State the blood parasite species.
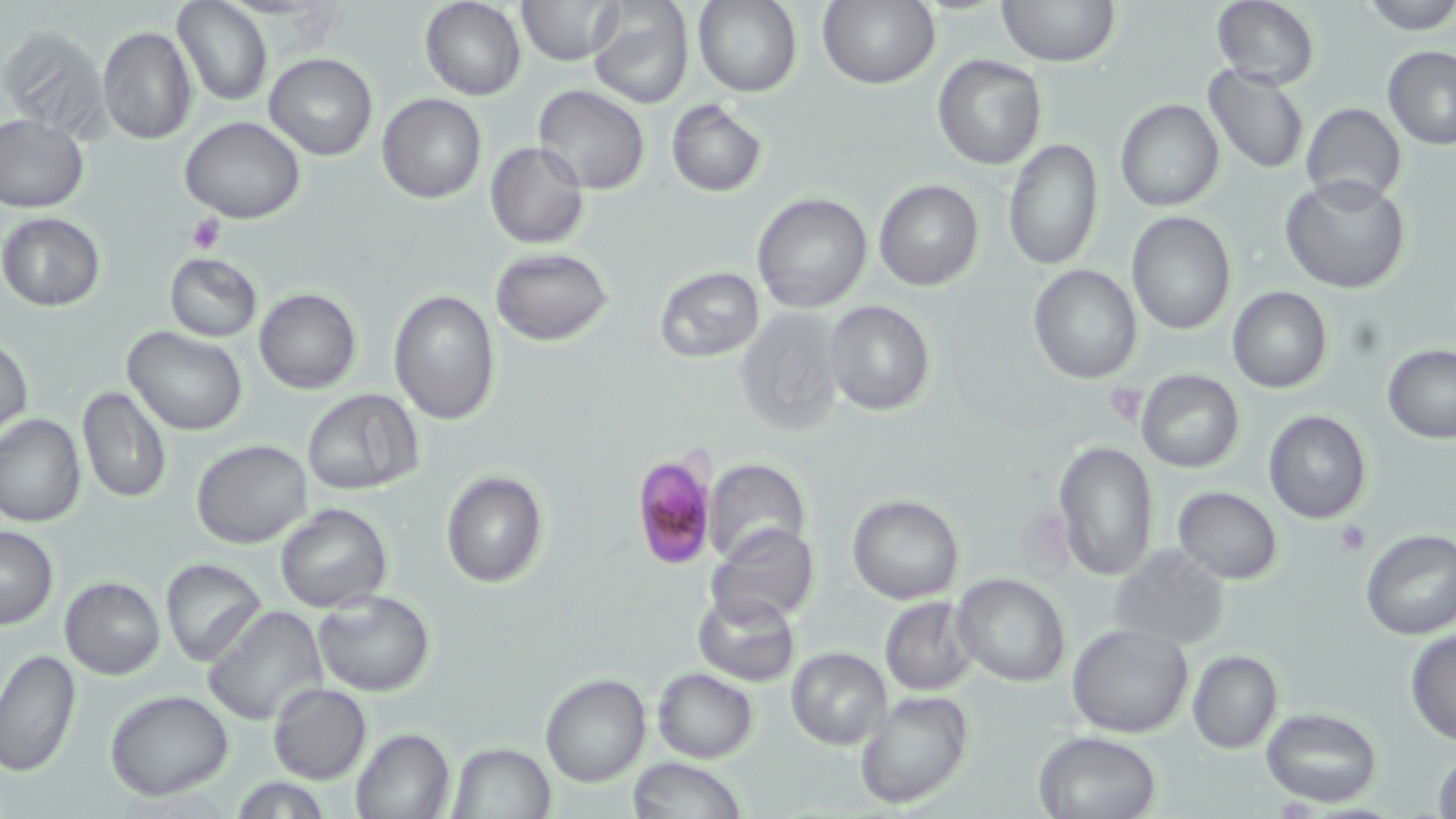
Plasmodium falciparum.

Approximate bounding boxes as (x1, y1, x2, y2) in pixels. Platelet locations: (186, 214, 224, 254), (1103, 384, 1144, 423), (1335, 518, 1370, 555). Plasmodium falciparum-infected red blood cell locations: (629, 451, 719, 572). Uninfected red blood cell locations: (173, 0, 272, 106), (517, 0, 620, 64), (586, 0, 694, 110), (693, 0, 802, 97), (820, 0, 939, 90), (998, 0, 1118, 66), (1211, 0, 1321, 90), (1357, 0, 1456, 35), (420, 1, 526, 100), (98, 24, 197, 145), (2, 25, 109, 137), (1382, 45, 1456, 148), (265, 52, 377, 159), (932, 54, 1046, 170), (1203, 65, 1308, 173), (532, 86, 650, 196), (377, 93, 486, 204), (665, 99, 768, 197), (1115, 99, 1224, 213), (1300, 104, 1406, 205), (0, 114, 89, 213), (179, 116, 306, 223), (1003, 138, 1104, 271), (485, 141, 589, 250), (1281, 175, 1411, 295), (874, 178, 985, 292), (751, 192, 872, 313), (1126, 210, 1236, 335), (0, 213, 105, 311), (490, 247, 614, 346), (164, 252, 262, 341), (1029, 264, 1143, 383), (652, 265, 766, 364), (253, 287, 361, 394), (1228, 287, 1331, 394), (387, 289, 500, 426), (824, 300, 934, 417), (735, 307, 846, 437), (123, 326, 248, 436), (0, 337, 33, 436), (1382, 345, 1456, 442), (1136, 369, 1244, 474), (76, 386, 172, 503), (302, 388, 423, 496), (1263, 411, 1370, 524), (1, 414, 86, 528), (1052, 437, 1157, 581), (192, 439, 311, 549), (703, 457, 811, 563), (440, 469, 550, 588), (1173, 486, 1283, 584), (847, 495, 963, 604), (275, 505, 391, 613), (709, 523, 821, 625), (0, 526, 59, 629), (1359, 528, 1456, 640), (1107, 545, 1232, 649), (159, 559, 267, 664), (953, 573, 1071, 688), (60, 575, 165, 678), (312, 589, 436, 696), (693, 590, 802, 685), (880, 597, 978, 695), (203, 605, 328, 728), (1066, 623, 1193, 739), (1404, 628, 1456, 744), (785, 646, 892, 749), (0, 649, 81, 778), (1187, 649, 1282, 755), (652, 669, 758, 762), (540, 674, 651, 787), (268, 683, 371, 784), (105, 690, 233, 800), (853, 691, 974, 810), (1261, 707, 1382, 806), (350, 727, 455, 818), (1033, 730, 1162, 819), (448, 742, 557, 818), (1432, 744, 1456, 819), (629, 756, 747, 819). Image is 1456×819 pixels. May-Grünwald-Giemsa-stained preparation. Captured at 1000x magnification. One field of a larger specimen. Thin blood smear. Optical microscopy.